Report the malaria status of this cell.
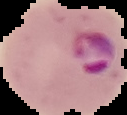

Parasitized.

{
  "image_size": "127×115 pixels",
  "preparation": "thin blood smear",
  "image_type": "segmented cell region with the area outside set to black"
}